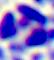
Captured at 400x magnification. A white blood cell is shown. Photomicrograph.